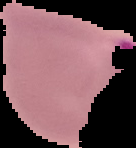
Summary:
  - Image size: 136×148 pixels
  - Preparation: thin blood smear
  - Malaria status: parasitized
  - Image type: cell region segmented out of the field of view; surrounding area masked to black